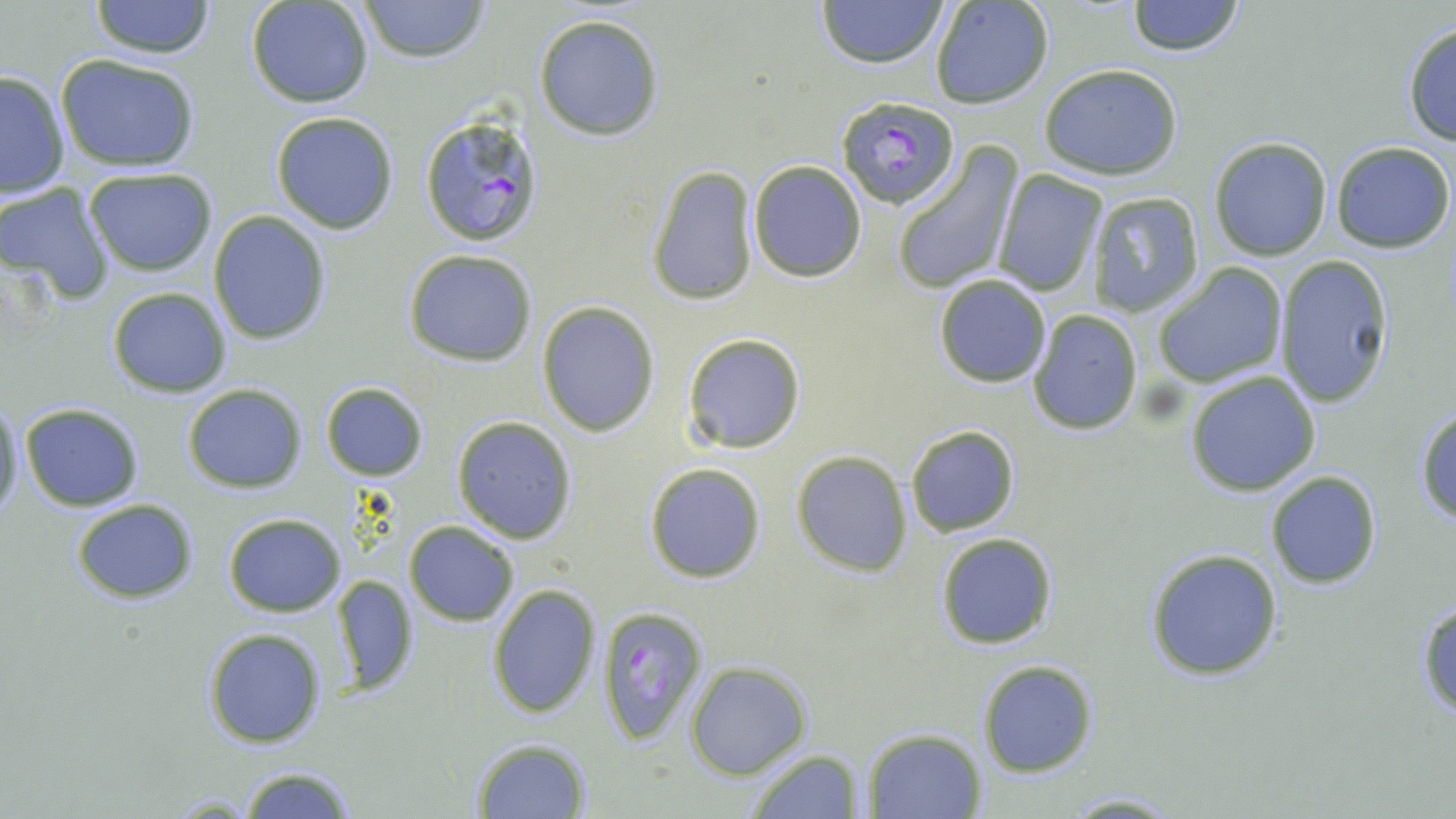 Approximate bounding boxes as named x1/y1/x2/y2 corners in pixels. Uninfected red blood cell locations: (x1=90, y1=0, x2=214, y2=60), (x1=815, y1=0, x2=949, y2=70), (x1=1127, y1=0, x2=1247, y2=56), (x1=246, y1=1, x2=374, y2=108), (x1=357, y1=1, x2=492, y2=63), (x1=930, y1=1, x2=1054, y2=110), (x1=534, y1=16, x2=664, y2=140), (x1=1400, y1=23, x2=1456, y2=147), (x1=55, y1=53, x2=201, y2=172), (x1=1039, y1=62, x2=1184, y2=181), (x1=0, y1=69, x2=70, y2=200), (x1=270, y1=112, x2=400, y2=233), (x1=1208, y1=136, x2=1333, y2=261), (x1=1329, y1=141, x2=1455, y2=254), (x1=891, y1=143, x2=1023, y2=297), (x1=747, y1=160, x2=868, y2=282), (x1=82, y1=166, x2=218, y2=276), (x1=648, y1=166, x2=758, y2=305), (x1=992, y1=170, x2=1107, y2=297), (x1=0, y1=183, x2=115, y2=303), (x1=1086, y1=192, x2=1209, y2=316), (x1=208, y1=211, x2=332, y2=345), (x1=403, y1=249, x2=538, y2=367), (x1=1275, y1=255, x2=1396, y2=408), (x1=1155, y1=263, x2=1287, y2=387), (x1=933, y1=276, x2=1051, y2=388), (x1=106, y1=287, x2=232, y2=398), (x1=536, y1=301, x2=660, y2=437), (x1=1026, y1=309, x2=1143, y2=434), (x1=682, y1=333, x2=807, y2=454), (x1=1185, y1=372, x2=1322, y2=497), (x1=319, y1=381, x2=429, y2=482), (x1=180, y1=383, x2=308, y2=494), (x1=0, y1=396, x2=24, y2=522), (x1=18, y1=402, x2=145, y2=512), (x1=1414, y1=405, x2=1456, y2=525), (x1=451, y1=416, x2=578, y2=543), (x1=904, y1=424, x2=1020, y2=536), (x1=791, y1=451, x2=914, y2=575), (x1=644, y1=461, x2=766, y2=583), (x1=1264, y1=470, x2=1382, y2=590), (x1=70, y1=499, x2=196, y2=603), (x1=222, y1=511, x2=347, y2=617), (x1=404, y1=520, x2=520, y2=626), (x1=935, y1=532, x2=1059, y2=649), (x1=1144, y1=548, x2=1284, y2=682), (x1=329, y1=575, x2=421, y2=697), (x1=486, y1=582, x2=603, y2=719), (x1=1415, y1=596, x2=1456, y2=721), (x1=201, y1=627, x2=328, y2=748), (x1=977, y1=659, x2=1098, y2=778), (x1=687, y1=662, x2=811, y2=779), (x1=863, y1=728, x2=986, y2=817), (x1=468, y1=737, x2=592, y2=817), (x1=743, y1=747, x2=867, y2=818), (x1=235, y1=764, x2=358, y2=818), (x1=1058, y1=790, x2=1187, y2=817). Plasmodium falciparum-infected red blood cell locations: (x1=836, y1=94, x2=960, y2=207), (x1=417, y1=112, x2=548, y2=248), (x1=595, y1=605, x2=706, y2=746). Slide-level diagnosis: Plasmodium falciparum. One field of a larger specimen. May-Grünwald-Giemsa-stained preparation. Thin blood film. Image is 1456×819 pixels. 1000x magnification. Optical microscopy.